Assess this cell for malaria.
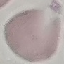
Uninfected.

image type = automatically extracted cell patch, resized to 64 × 64 pixels
capture = smartphone camera at the microscope eyepiece
stain = Giemsa
preparation = thin blood film